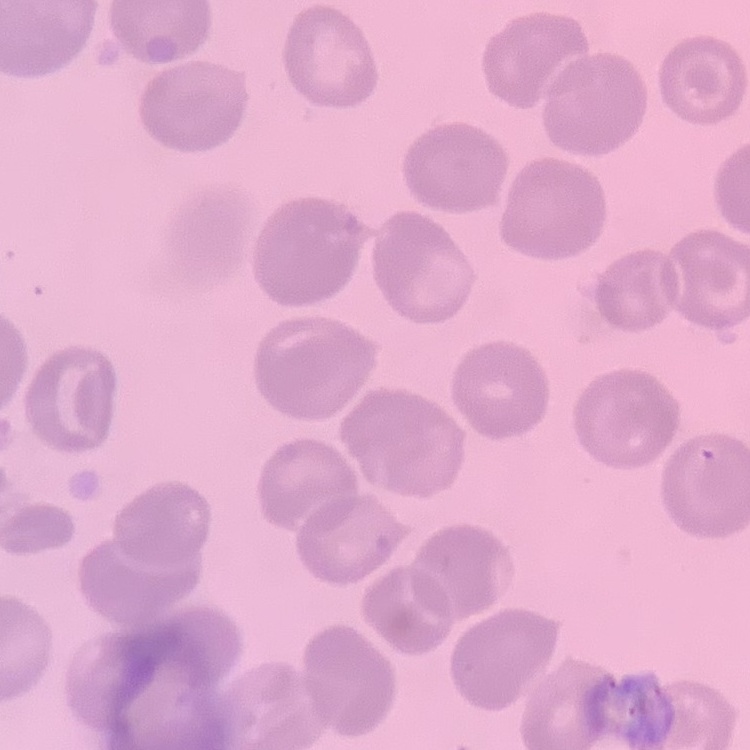
red blood cell morphology = no rouleaux formation
stain = Field's or Giemsa
preparation = thin peripheral smear
image type = one tile cut from a larger photomicrograph